Identify the preparation type.
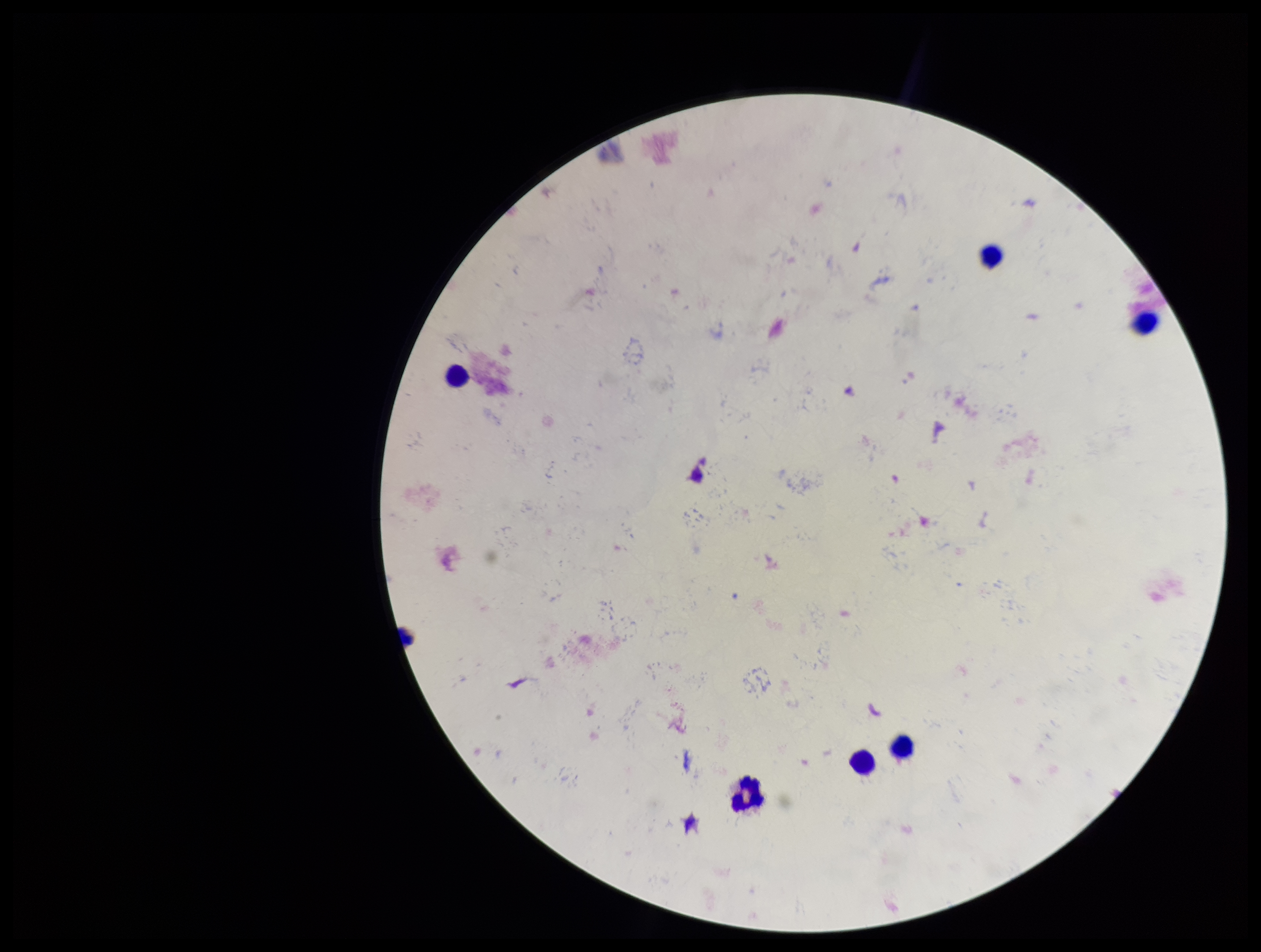

It is a thick blood smear.

Image is 1261×952 pixels. Parasite count: 0. Giemsa stain. Plasmodium parasites: none detected. Smartphone photograph taken through the eyepiece of a microscope. Single field of view. Leukocyte count: 6. Patient malaria status: negative.